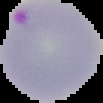

Summary:
  - Image type: cell region segmented out of the field of view; surrounding area masked to black
  - Image size: 103×103 pixels
  - Result: Plasmodium parasites detected
  - Preparation: thin blood film